Draw a bounding box around every malaria parasite.
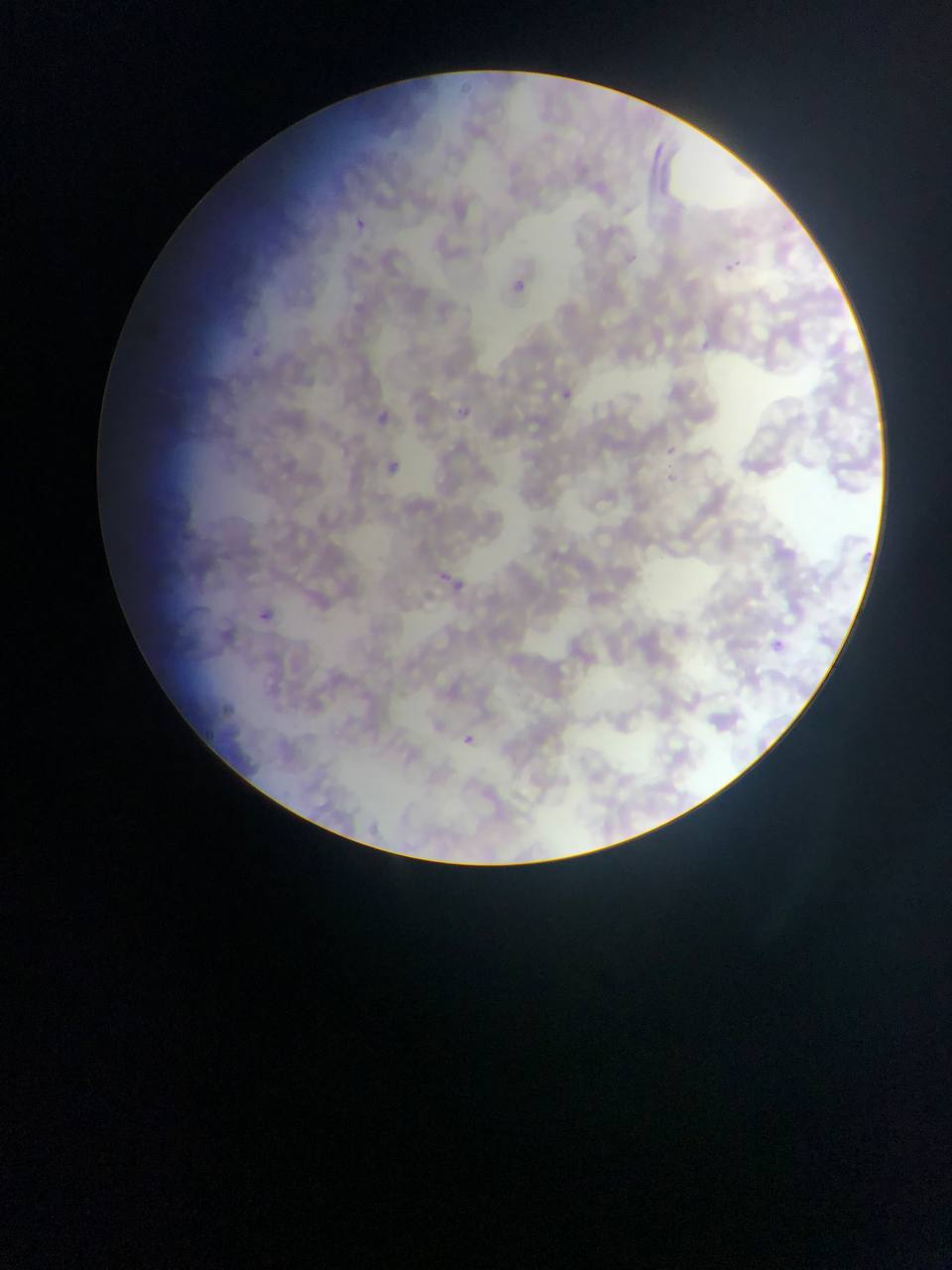
Approximate bounding boxes as (left, top, right, bottom) in pixels.
Malaria parasites: (355, 220, 365, 228), (626, 253, 636, 263), (720, 254, 744, 274), (515, 280, 525, 291), (697, 337, 719, 351), (243, 340, 268, 364), (562, 389, 573, 400), (452, 400, 474, 419), (366, 404, 401, 425), (661, 443, 683, 458), (389, 461, 400, 471), (666, 472, 676, 482), (439, 566, 455, 583), (454, 581, 462, 591), (259, 612, 269, 620), (773, 639, 784, 649), (219, 702, 244, 716), (464, 734, 477, 745).

country = Ghana
capture = mobile-phone photograph through a microscope
field of view = single
preparation = thin blood film
image size = 952×1270 pixels